Locate malaria parasites and leukocytes.
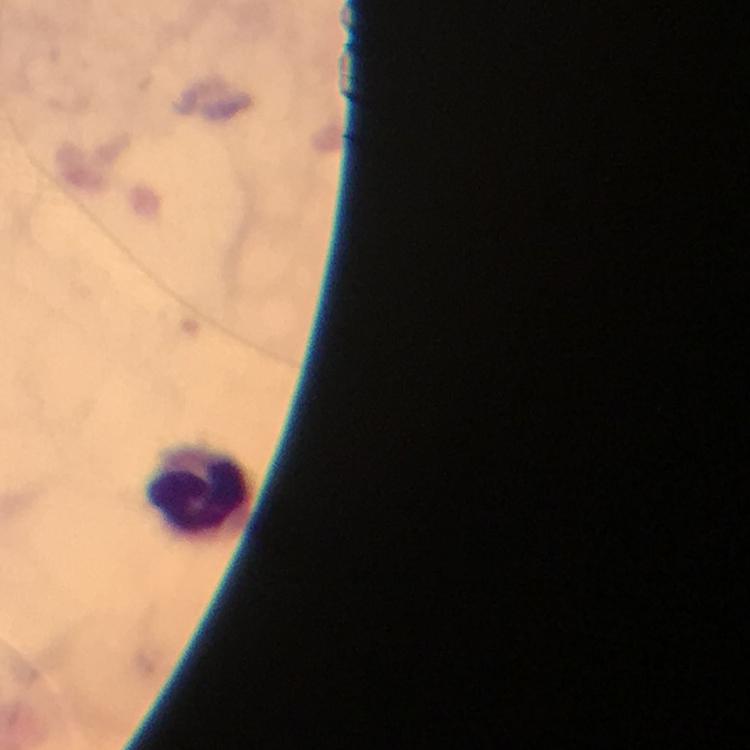

No malaria parasites detected.
Approximate centers as (x, y) in pixels.
Leukocytes: (202, 489).

image size = 750×750 pixels
magnification = 100x
immersion oil = applied
capture = smartphone camera through the microscope
cropped from = one field of view
context = from a diagnostic examination for malaria
preparation = thick smear
stain = Giemsa